State the blood parasite species.
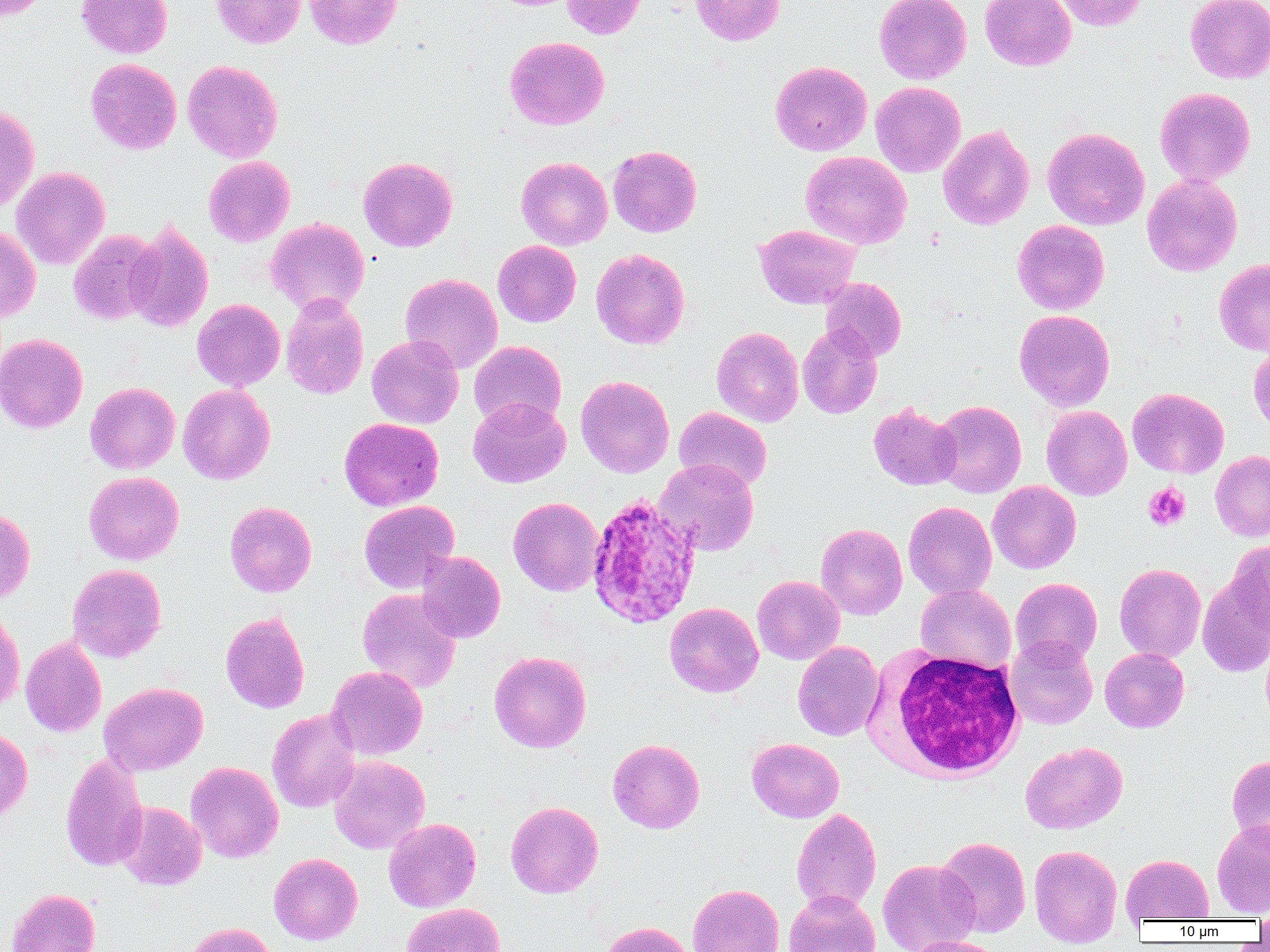

Plasmodium ovale.

Summary:
  - Coordinate format: approximate bounding boxes as named x1/y1/x2/y2 corners in pixels
  - White blood cell locations: (x1=875, y1=648, x2=1027, y2=781)
  - Plasmodium ovale-infected red blood cell locations: (x1=586, y1=493, x2=702, y2=629)
  - Uninfected red blood cell locations: (x1=0, y1=0, x2=49, y2=21), (x1=76, y1=0, x2=173, y2=59), (x1=211, y1=0, x2=306, y2=48), (x1=304, y1=0, x2=402, y2=49), (x1=561, y1=0, x2=646, y2=39), (x1=691, y1=0, x2=785, y2=45), (x1=874, y1=0, x2=972, y2=84), (x1=980, y1=0, x2=1076, y2=71), (x1=1054, y1=0, x2=1148, y2=31), (x1=1185, y1=1, x2=1270, y2=83), (x1=504, y1=36, x2=609, y2=130), (x1=85, y1=58, x2=182, y2=154), (x1=182, y1=60, x2=283, y2=163), (x1=770, y1=61, x2=872, y2=155), (x1=871, y1=82, x2=966, y2=177), (x1=1155, y1=87, x2=1255, y2=186), (x1=0, y1=104, x2=40, y2=213), (x1=938, y1=125, x2=1034, y2=230), (x1=1042, y1=127, x2=1149, y2=230), (x1=607, y1=145, x2=702, y2=237), (x1=801, y1=151, x2=912, y2=249), (x1=203, y1=156, x2=295, y2=246), (x1=358, y1=156, x2=458, y2=252), (x1=516, y1=157, x2=613, y2=250), (x1=11, y1=166, x2=110, y2=269), (x1=1142, y1=174, x2=1243, y2=276), (x1=265, y1=217, x2=370, y2=315), (x1=1012, y1=219, x2=1110, y2=314), (x1=125, y1=221, x2=214, y2=332), (x1=754, y1=224, x2=861, y2=309), (x1=0, y1=225, x2=41, y2=322), (x1=68, y1=230, x2=162, y2=325), (x1=493, y1=240, x2=581, y2=327), (x1=591, y1=248, x2=690, y2=349), (x1=1214, y1=258, x2=1270, y2=356), (x1=400, y1=273, x2=502, y2=373), (x1=820, y1=277, x2=906, y2=361), (x1=281, y1=295, x2=369, y2=400), (x1=192, y1=298, x2=285, y2=391), (x1=1014, y1=309, x2=1115, y2=411), (x1=797, y1=325, x2=882, y2=419), (x1=711, y1=327, x2=803, y2=427), (x1=0, y1=333, x2=88, y2=433), (x1=366, y1=334, x2=464, y2=429), (x1=468, y1=341, x2=566, y2=430), (x1=1248, y1=342, x2=1270, y2=432), (x1=575, y1=375, x2=674, y2=478), (x1=85, y1=382, x2=180, y2=474), (x1=178, y1=384, x2=275, y2=484), (x1=1127, y1=387, x2=1229, y2=478), (x1=468, y1=397, x2=570, y2=487), (x1=931, y1=400, x2=1026, y2=498), (x1=868, y1=402, x2=961, y2=490), (x1=1041, y1=405, x2=1132, y2=500), (x1=673, y1=407, x2=772, y2=492), (x1=339, y1=417, x2=444, y2=511), (x1=1210, y1=450, x2=1270, y2=541), (x1=654, y1=459, x2=758, y2=556), (x1=84, y1=471, x2=184, y2=565), (x1=987, y1=481, x2=1081, y2=573), (x1=508, y1=497, x2=604, y2=596), (x1=359, y1=500, x2=459, y2=593), (x1=224, y1=501, x2=317, y2=597), (x1=903, y1=501, x2=997, y2=599), (x1=0, y1=508, x2=35, y2=604), (x1=816, y1=523, x2=907, y2=619), (x1=1225, y1=541, x2=1270, y2=632), (x1=417, y1=551, x2=505, y2=642), (x1=1114, y1=563, x2=1206, y2=662), (x1=67, y1=564, x2=166, y2=662), (x1=1010, y1=574, x2=1206, y2=661), (x1=1197, y1=574, x2=1270, y2=677), (x1=752, y1=575, x2=844, y2=665), (x1=1010, y1=577, x2=1102, y2=667), (x1=915, y1=583, x2=1016, y2=674), (x1=358, y1=589, x2=462, y2=693), (x1=664, y1=602, x2=764, y2=697), (x1=0, y1=609, x2=25, y2=714), (x1=220, y1=611, x2=310, y2=713), (x1=20, y1=636, x2=107, y2=737), (x1=1005, y1=636, x2=1098, y2=729), (x1=792, y1=641, x2=884, y2=741), (x1=1100, y1=648, x2=1189, y2=732), (x1=489, y1=651, x2=591, y2=753), (x1=327, y1=666, x2=427, y2=760), (x1=99, y1=682, x2=208, y2=775), (x1=267, y1=708, x2=361, y2=813), (x1=0, y1=728, x2=32, y2=823), (x1=747, y1=738, x2=844, y2=823), (x1=607, y1=739, x2=705, y2=833), (x1=1021, y1=741, x2=1127, y2=833), (x1=60, y1=752, x2=149, y2=872), (x1=1227, y1=755, x2=1270, y2=847), (x1=329, y1=756, x2=429, y2=854), (x1=185, y1=761, x2=283, y2=862), (x1=115, y1=801, x2=207, y2=890), (x1=505, y1=801, x2=603, y2=898), (x1=791, y1=808, x2=881, y2=914), (x1=383, y1=818, x2=481, y2=912), (x1=1212, y1=820, x2=1270, y2=918), (x1=936, y1=837, x2=1031, y2=937), (x1=1029, y1=844, x2=1122, y2=947), (x1=268, y1=853, x2=362, y2=944), (x1=1121, y1=854, x2=1213, y2=922), (x1=877, y1=859, x2=979, y2=952), (x1=687, y1=883, x2=784, y2=952), (x1=6, y1=888, x2=101, y2=952), (x1=783, y1=890, x2=881, y2=952), (x1=401, y1=902, x2=506, y2=952), (x1=1254, y1=906, x2=1270, y2=940), (x1=599, y1=921, x2=694, y2=952), (x1=181, y1=922, x2=277, y2=952), (x1=903, y1=935, x2=1004, y2=952)
  - Platelet locations: (x1=1143, y1=483, x2=1190, y2=531)
  - Magnification: 1000x
  - Preparation: thin blood film
  - Modality: optical microscopy
  - Field of view: single
  - Image size: 1270×952 pixels